State which parasite is depicted.
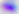

This is Toxoplasma gondii.

Summary:
  - Magnification: 400x
  - Modality: photomicrograph